Classify this cell by malaria status.
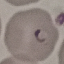

It is parasitized.

capture: smartphone through the microscope eyepiece
preparation: thin blood smear
image_type: automatically extracted cell patch, resized to 64 × 64 pixels
stain: Giemsa